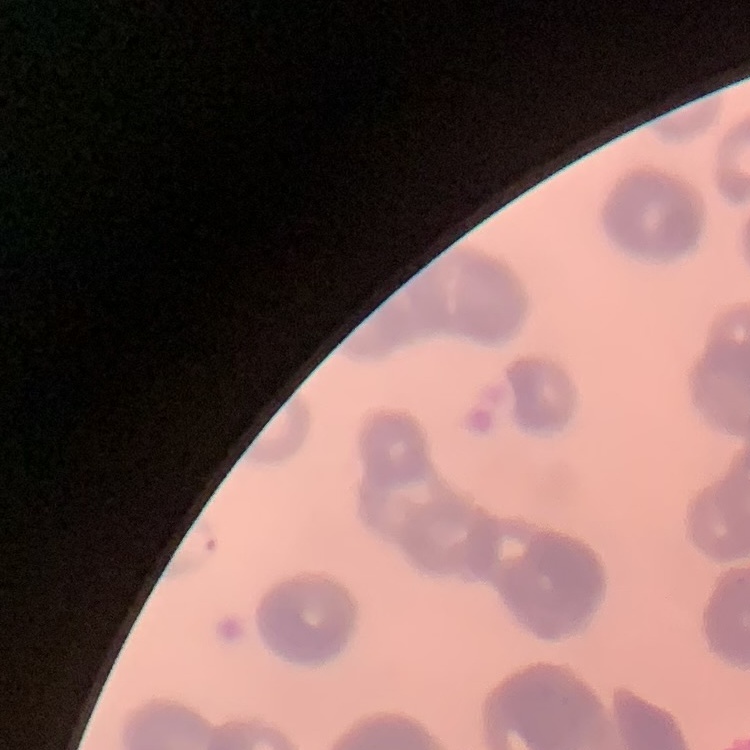
Summary:
  - Red blood cell morphology: rouleaux formation
  - Stain: Field's or Giemsa
  - Preparation: thin blood smear
  - Image type: square crop of a larger photomicrograph